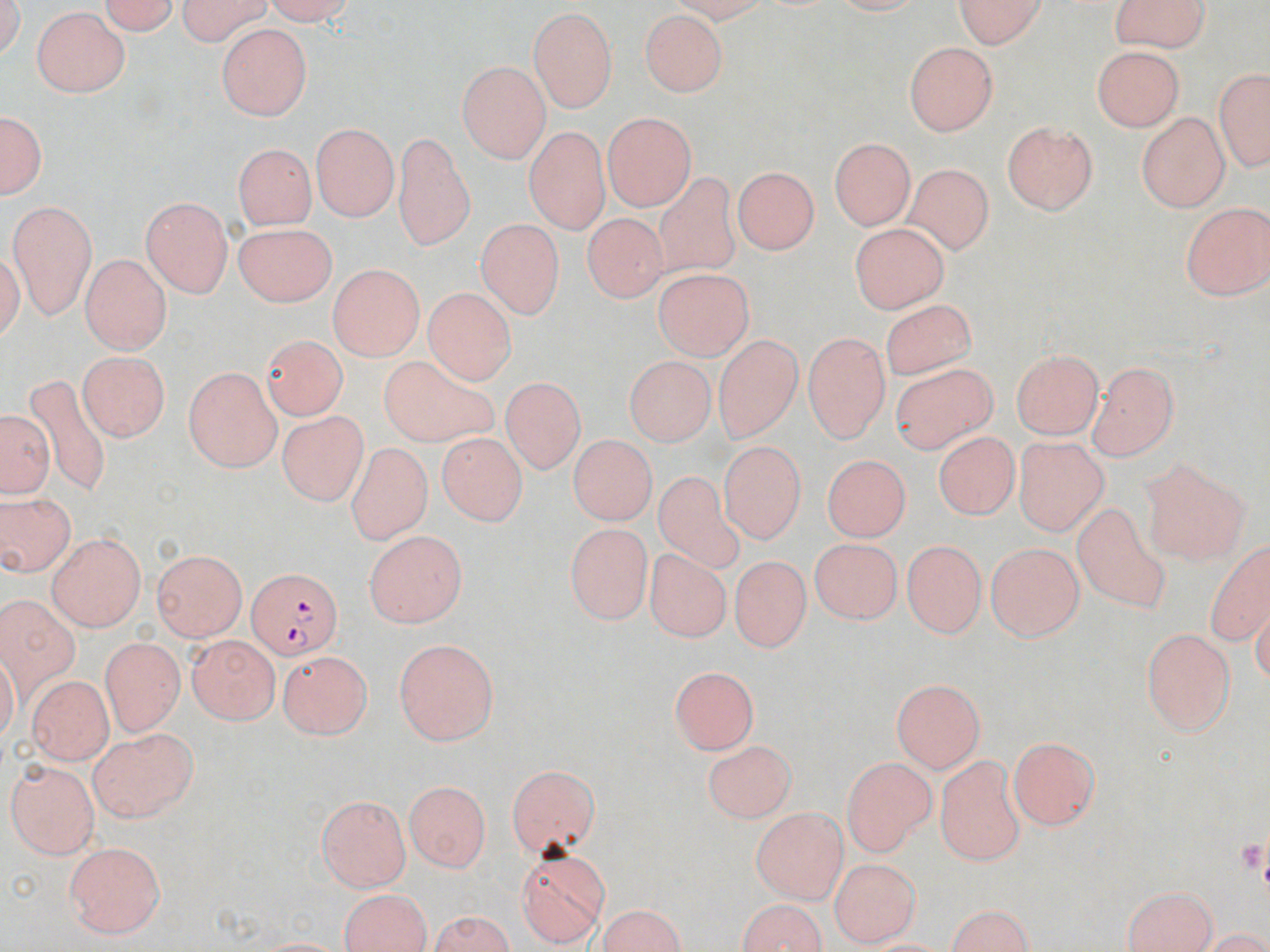

slide-level diagnosis = Plasmodium falciparum
preparation = thin blood film
magnification = 1000x
field of view = one of a larger specimen
Plasmodium falciparum-infected red blood cell locations = approximate bounding boxes as [x1, y1, x2, y2] in pixels: [248, 568, 341, 662]
modality = optical microscopy
uninfected red blood cell locations = approximate bounding boxes as [x1, y1, x2, y2] in pixels: [94, 0, 180, 34], [171, 0, 278, 40], [258, 0, 355, 25], [1112, 0, 1211, 47], [952, 1, 1050, 45], [633, 5, 728, 100], [526, 6, 620, 113], [32, 8, 134, 98], [217, 22, 309, 121], [904, 39, 1002, 135], [1092, 44, 1187, 130], [455, 61, 551, 160], [1211, 66, 1269, 171], [0, 105, 49, 202], [602, 113, 697, 210], [1136, 113, 1227, 212], [1001, 121, 1101, 215], [309, 124, 399, 223], [524, 125, 613, 239], [395, 134, 473, 251], [830, 136, 919, 231], [233, 141, 316, 227], [907, 161, 991, 252], [732, 167, 821, 257], [647, 170, 747, 285], [141, 196, 234, 296], [8, 199, 97, 317], [1180, 199, 1269, 297], [581, 211, 668, 304], [475, 216, 560, 322], [229, 218, 334, 305], [852, 224, 946, 316], [79, 255, 170, 355], [328, 258, 423, 360], [653, 271, 757, 364], [424, 288, 515, 385], [876, 304, 986, 382], [801, 327, 890, 440], [260, 333, 349, 416], [715, 336, 805, 446], [1010, 349, 1105, 439], [76, 350, 169, 441], [378, 351, 500, 451], [890, 359, 996, 455], [1091, 359, 1180, 459], [623, 361, 716, 449], [182, 368, 282, 471], [24, 370, 116, 494], [502, 377, 584, 476], [3, 409, 51, 498], [279, 411, 365, 506], [933, 428, 1020, 528], [1015, 432, 1107, 537], [437, 435, 525, 527], [566, 438, 654, 528], [719, 443, 806, 546], [344, 444, 433, 542], [821, 452, 908, 545], [1137, 453, 1249, 567], [653, 473, 743, 575], [1, 493, 74, 578], [1069, 503, 1179, 621], [565, 526, 652, 623], [362, 532, 465, 629], [46, 534, 148, 631], [1201, 537, 1270, 646], [808, 538, 904, 628], [901, 539, 985, 637], [983, 544, 1084, 642], [152, 548, 244, 642], [647, 550, 728, 645], [734, 559, 807, 654], [0, 593, 84, 714], [1139, 628, 1239, 737], [188, 636, 280, 723], [392, 638, 500, 745], [100, 639, 182, 734], [280, 648, 370, 738], [30, 658, 178, 752], [672, 666, 756, 754], [25, 672, 112, 763], [890, 678, 988, 772], [89, 729, 198, 822], [1006, 736, 1102, 830], [704, 738, 795, 819], [937, 754, 1025, 866], [842, 756, 932, 858], [6, 759, 101, 856], [505, 764, 603, 861], [404, 778, 490, 870], [315, 795, 411, 892], [752, 806, 846, 904], [65, 842, 165, 937], [515, 847, 612, 944], [832, 860, 917, 944], [1118, 885, 1220, 952], [336, 888, 436, 951], [730, 896, 832, 952], [940, 902, 1038, 952], [593, 904, 690, 952], [423, 913, 518, 950]
stain = May-Grünwald-Giemsa
image size = 1270×952 pixels